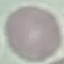
Summary:
  - Result: no malaria parasites seen
  - Image type: automatically extracted cell patch, resized to 64 × 64 pixels
  - Stain: Giemsa
  - Preparation: thin blood film
  - Capture: smartphone through the microscope eyepiece